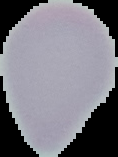
image size = 118×157 pixels
preparation = thin blood film
image type = segmented cell region with the area outside set to black
malaria status = uninfected